Assess this cell for malaria.
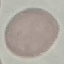
Uninfected.

Summary:
  - Image type: automatically extracted cell patch, resized to 64 × 64 pixels
  - Stain: Giemsa
  - Preparation: thin blood smear
  - Capture: smartphone through the microscope eyepiece